Report the malaria status of this cell.
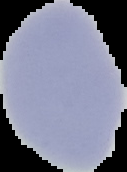

Uninfected.

image size = 127×172 pixels
image type = segmented cell region on a black background
preparation = thin blood film